Report the malaria status of this cell.
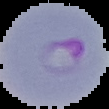
It is parasitized.

image size = 109×109 pixels
preparation = thin blood smear
image type = segmented cell region on a black background